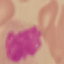

Result: no malaria parasites seen. Automatically extracted cell patch, resized to 64 × 64 pixels. Photographed with a smartphone camera at the microscope eyepiece. Giemsa stain. Thin blood smear.